Give the position of every Plasmodium parasite, noting whether each is a trophozoite, schizont, or gametocyte.
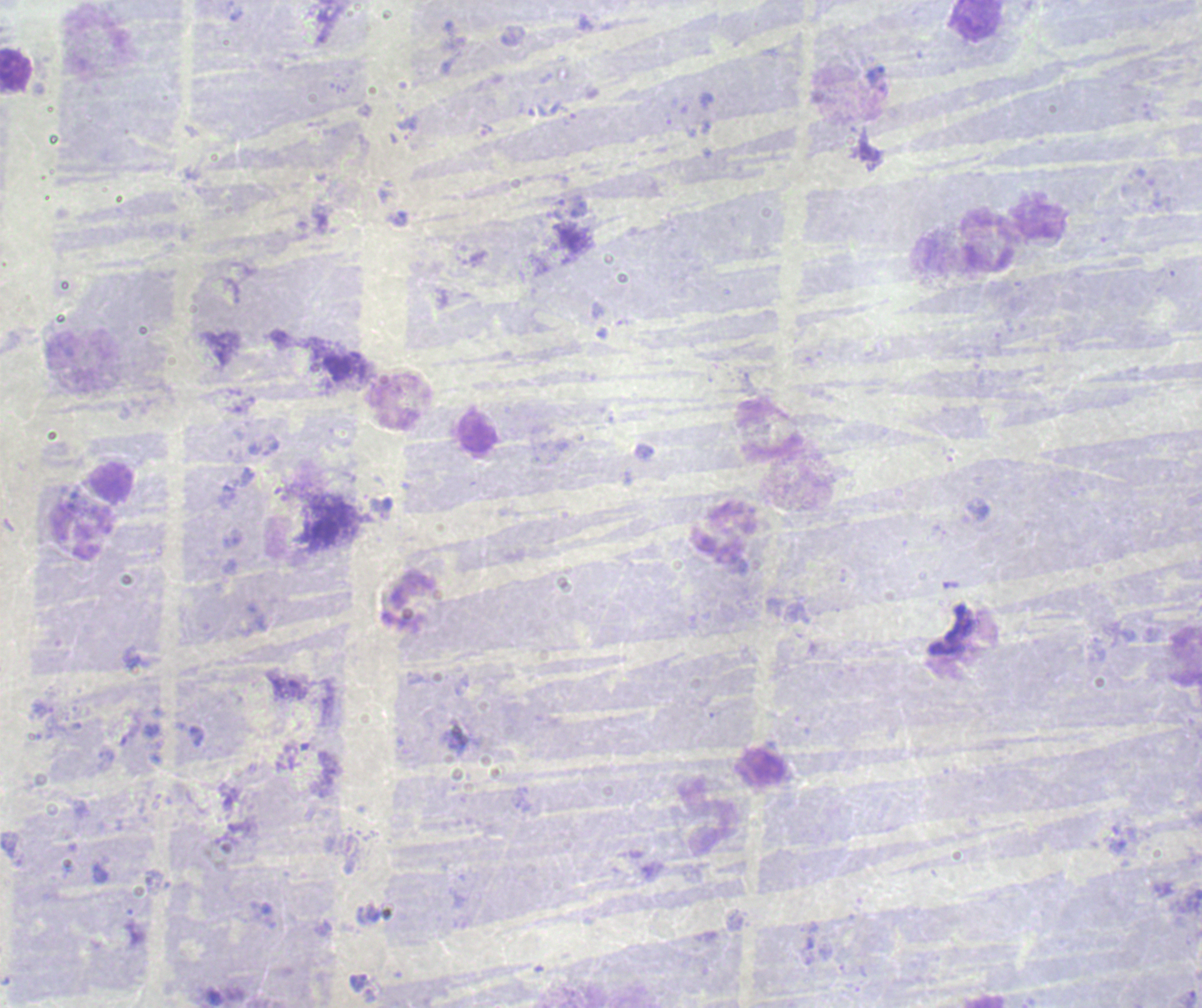

Approximate object centers, in pixels from the top-left corner.
Trophozoites: (x=875, y=75).
No schizont or gametocyte forms observed.

coordinate format = approximate object centers, in pixels from the top-left corner
leukocyte locations = (x=976, y=21), (x=15, y=71), (x=989, y=243), (x=397, y=402), (x=479, y=431), (x=81, y=529), (x=723, y=534), (x=709, y=819)
background quality = poor
context = previously used in a real diagnosis
field of view = single
magnification = 100x
preparation = thick blood smear
stain = Romanowsky
image size = 1202×1008 pixels